Classify this cell by malaria status.
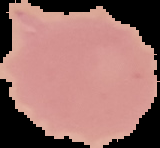
Uninfected.

{
  "image_size": "160×148 pixels",
  "image_type": "segmented cell region with the area outside set to black",
  "preparation": "thin blood film"
}